Assess the morphology of the erythrocytes.
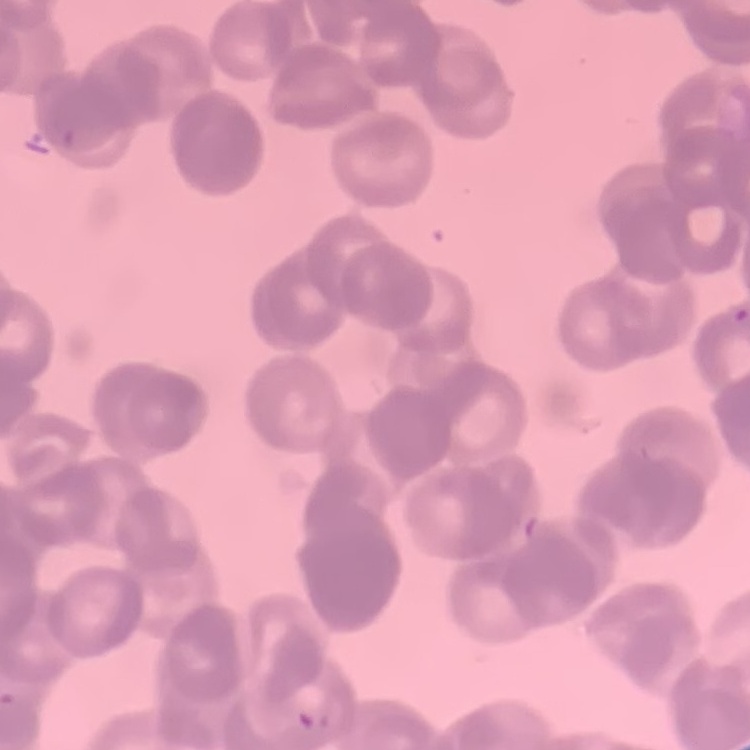
Rouleaux formation.

Thin blood smear. One tile cut from a larger photomicrograph. Field's or Giemsa stain.